Comment on the morphology of the red blood cells.
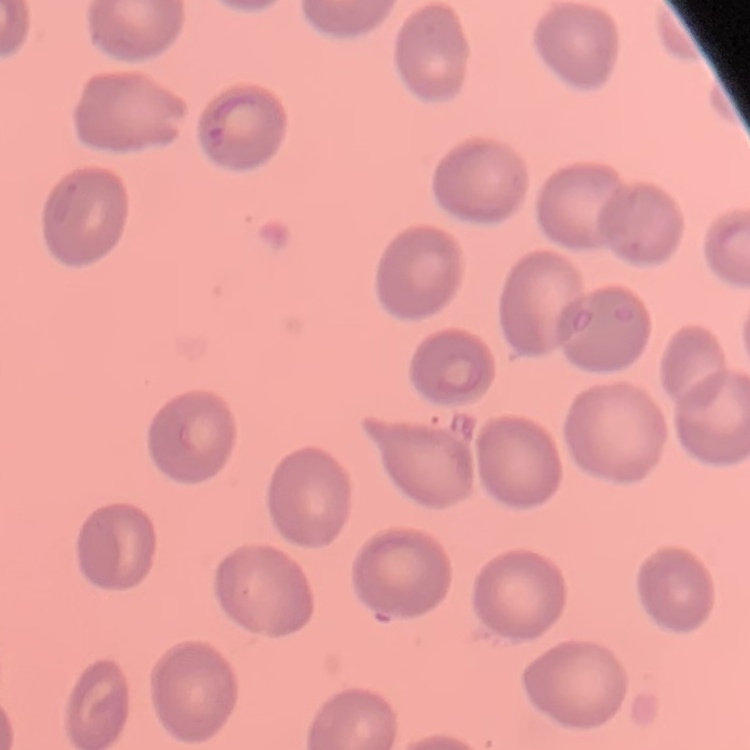

They show no rouleaux formation.

stain = Field's or Giemsa
image type = one tile cut from a larger photomicrograph
preparation = thin peripheral smear